Locate every blood parasite and identify its species.
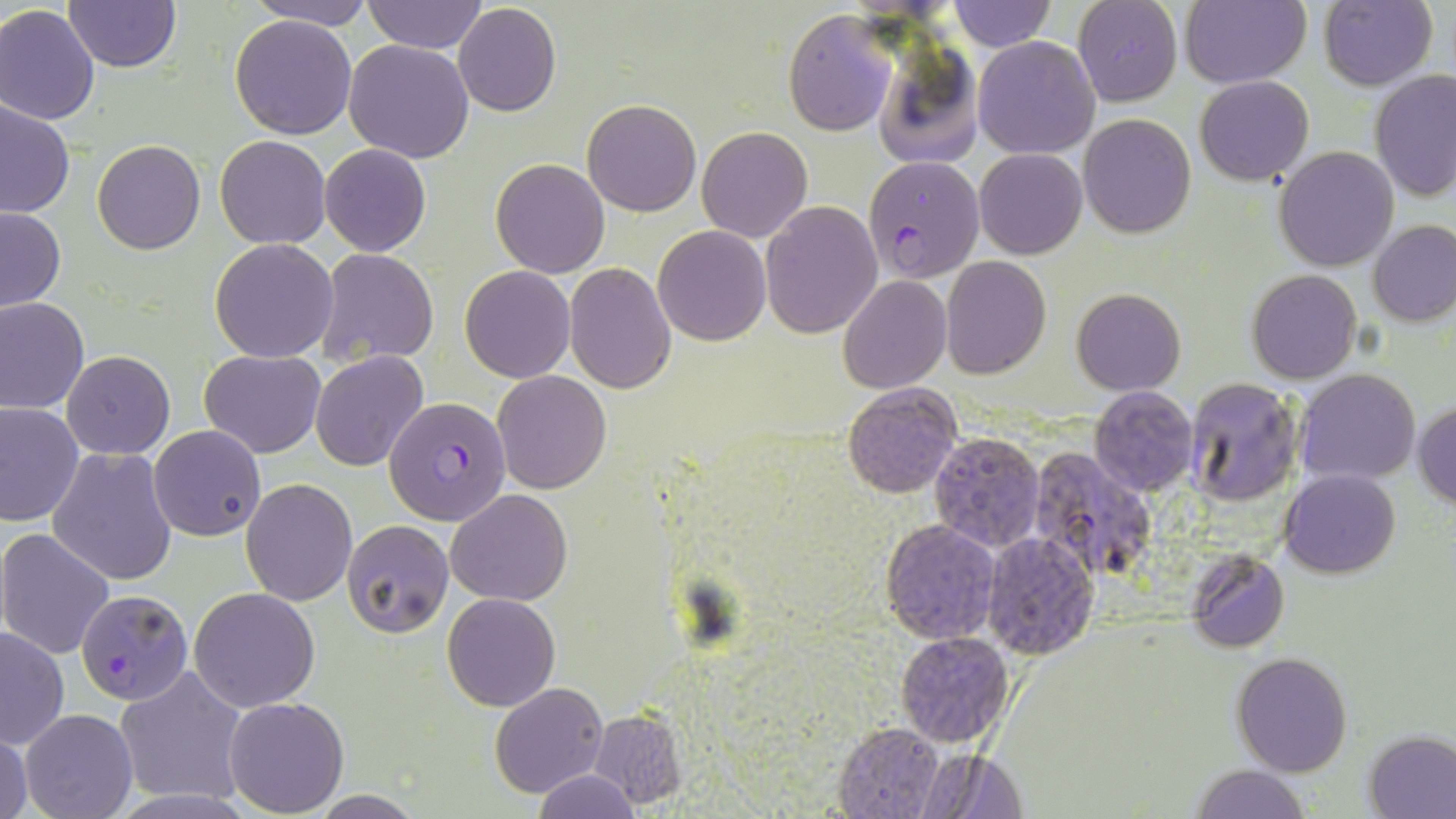
Approximate bounding boxes as (x1,y1)-(x2,y2) corner pairs in pixels.
Plasmodium falciparum-infected red blood cells: (862,156)-(985,282), (383,395)-(510,526), (1028,444)-(1157,581), (76,590)-(194,704).
No Plasmodium ovale, Plasmodium malariae, Plasmodium vivax, Babesia divergens, or Trypanosoma brucei observed.

Uninfected red blood cell locations: (246,0)-(375,29), (363,0)-(487,54), (946,0)-(1055,51), (1073,0)-(1182,107), (1181,0)-(1311,87), (1318,0)-(1437,91), (64,1)-(181,73), (0,4)-(101,124), (453,4)-(561,117), (785,9)-(897,136), (229,13)-(358,139), (973,35)-(1100,159), (344,40)-(475,164), (870,44)-(984,171), (1370,69)-(1455,205), (1194,75)-(1313,185), (0,99)-(74,217), (582,99)-(701,217), (1078,114)-(1196,239), (697,126)-(813,242), (215,135)-(331,249), (93,139)-(206,254), (320,144)-(432,256), (1274,147)-(1399,271), (974,149)-(1087,259), (491,158)-(610,278), (760,202)-(883,339), (1,206)-(66,313), (1369,220)-(1456,326), (652,225)-(772,346), (209,239)-(338,362), (315,249)-(438,368), (941,257)-(1051,377), (566,261)-(677,395), (460,266)-(575,382), (1245,270)-(1361,384), (839,276)-(951,394), (1072,287)-(1186,395), (1,297)-(90,415), (200,348)-(327,457), (60,351)-(176,459), (311,351)-(429,472), (1295,368)-(1421,483), (492,371)-(611,494), (1184,377)-(1303,507), (841,384)-(961,498), (1089,387)-(1198,495), (1412,400)-(1456,509), (0,402)-(84,528), (148,424)-(266,541), (929,430)-(1046,553), (47,447)-(178,587), (1281,469)-(1400,578), (240,479)-(358,605), (448,489)-(571,606), (341,519)-(453,639), (880,519)-(1000,643), (0,527)-(115,660), (981,532)-(1101,659), (1186,548)-(1290,653), (189,587)-(320,713), (443,592)-(561,710), (1,627)-(70,749), (896,631)-(1015,746), (1231,652)-(1354,776), (114,666)-(248,807), (491,683)-(609,797), (222,697)-(349,816), (20,709)-(138,819), (587,713)-(686,808), (832,720)-(944,819), (1,727)-(33,819), (1363,729)-(1455,819), (914,746)-(1027,817), (1187,764)-(1309,819), (532,770)-(642,818), (308,791)-(428,819). Slide-level diagnosis: Plasmodium falciparum. Image is 1456×819 pixels. Thin blood smear. 1000x magnification. One field of a larger specimen. Light microscopy. May-Grünwald-Giemsa-stained preparation.